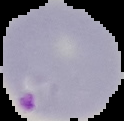
{
  "image_size": "124×121 pixels",
  "image_type": "segmented cell region on a black background",
  "result": "Plasmodium parasites identified",
  "preparation": "thin blood smear"
}